Comment on the morphology of the red blood cells.
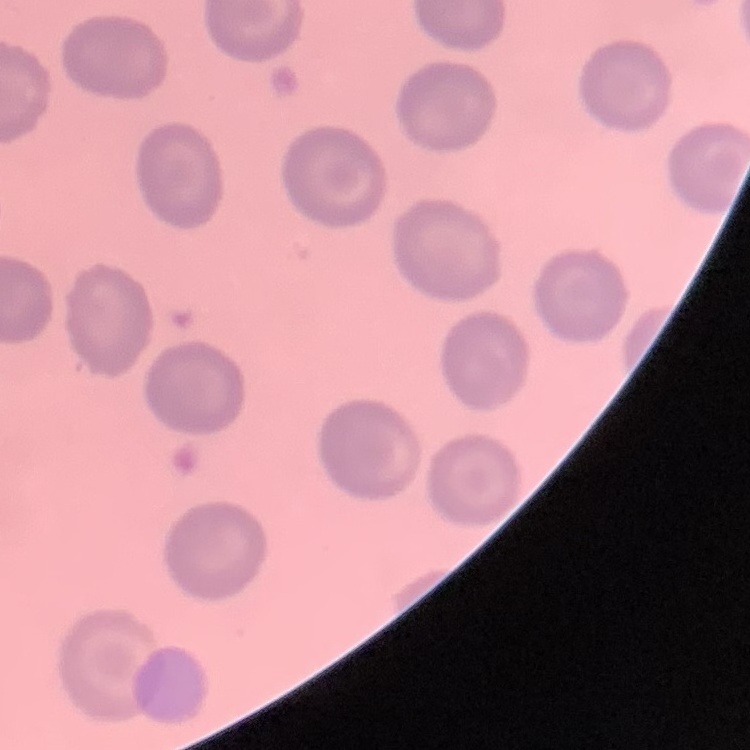
No rouleaux formation.

Summary:
  - Stain: Field's or Giemsa
  - Preparation: thin blood film
  - Image type: square crop of a larger photomicrograph